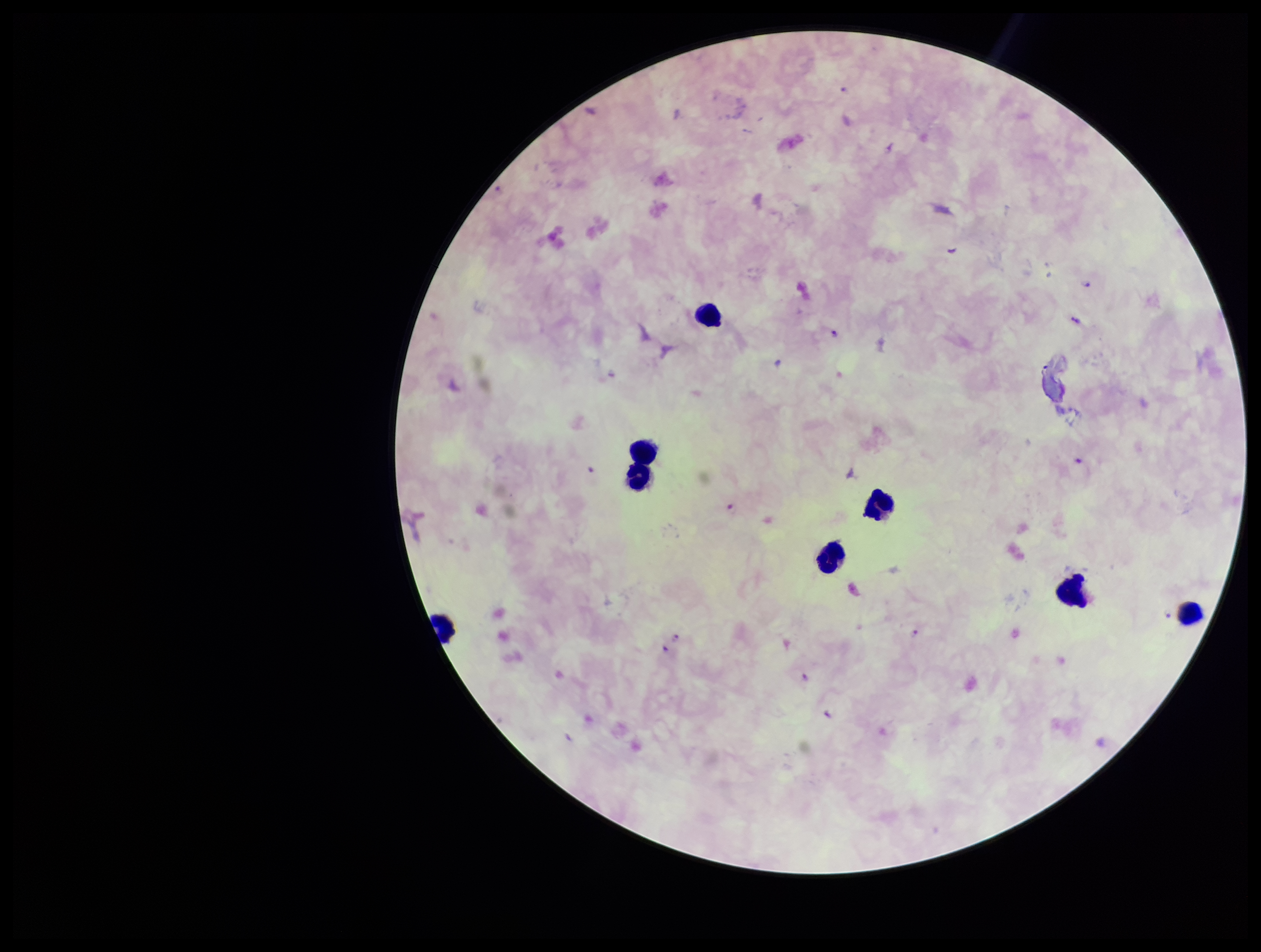
Summary:
  - Plasmodium parasites: detected
  - Leukocyte count: 8
  - Patient malaria status: positive
  - Species reported for this patient: Plasmodium falciparum
  - Preparation: thick blood smear
  - Stain: Giemsa
  - Parasite count: 11
  - Capture: smartphone photograph through the microscope eyepiece
  - Image size: 1261×952 pixels
  - Field of view: one from this slide